Classify this cell by malaria status.
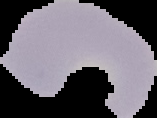
Uninfected.

From a thin blood smear. Cell region segmented out of the field of view; the surrounding area is masked to black. Image is 157×118 pixels.